Report the malaria status of this cell.
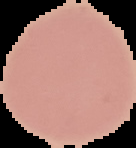

Uninfected.

image type = segmented cell region on a black background
image size = 136×148 pixels
preparation = thin blood film